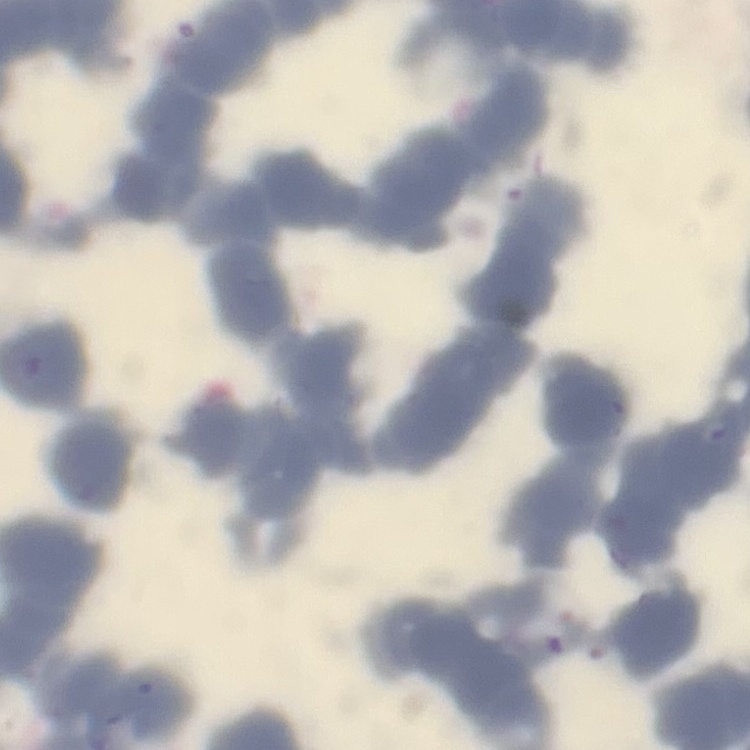
The erythrocytes show rouleaux formation. Square crop of a larger photomicrograph. Thin blood film. Stained with either Field's or Giemsa.